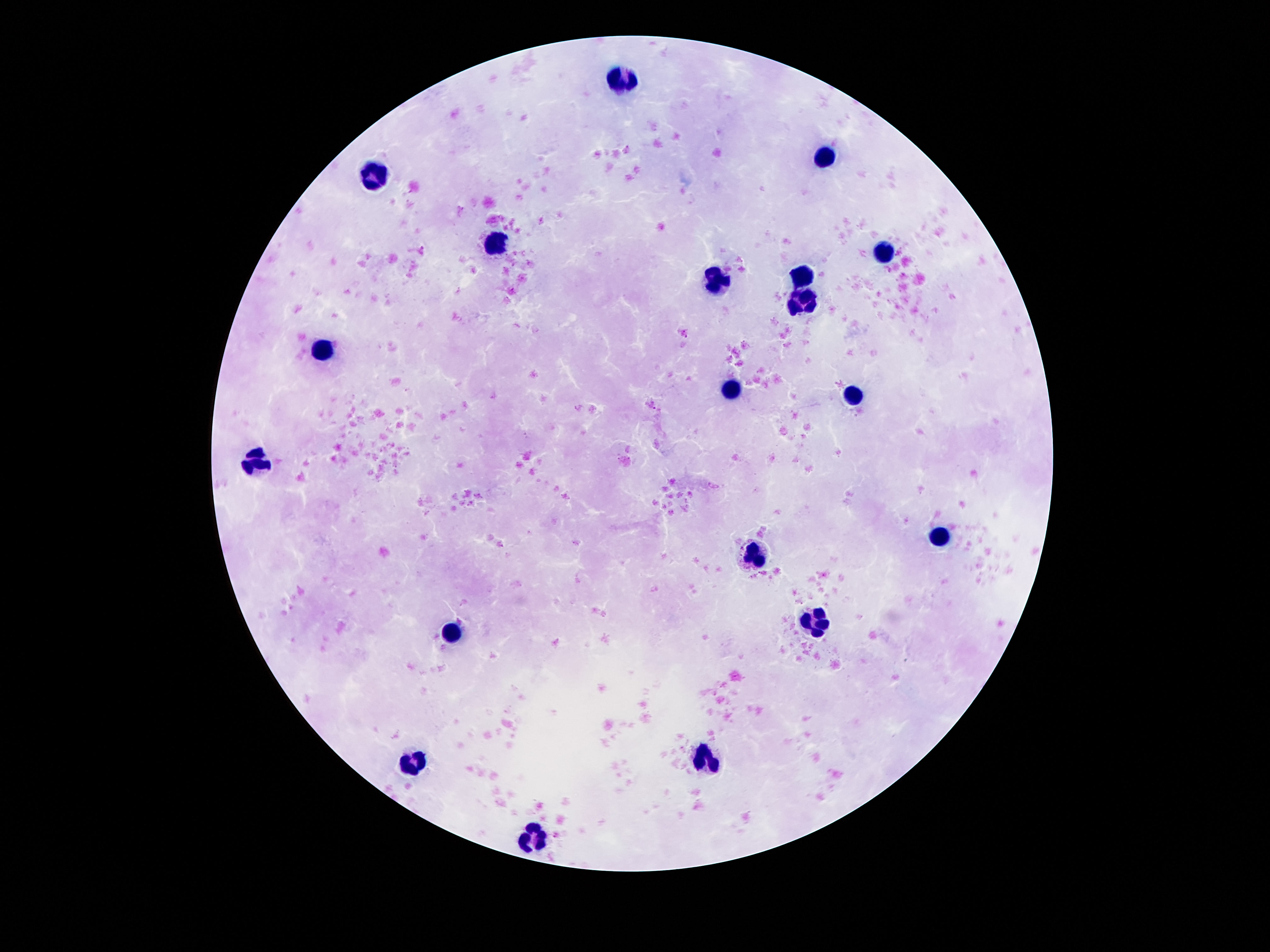

Approximate centers as {x, y} in pixels. Leukocyte locations: {622, 77}, {826, 160}, {375, 173}, {495, 242}, {885, 253}, {801, 274}, {715, 282}, {803, 300}, {325, 346}, {731, 387}, {853, 394}, {259, 460}, {944, 538}, {755, 554}, {815, 620}, {454, 632}, {706, 759}, {413, 766}, {529, 840}. Patient malaria status: uninfected. 100x magnification. Thick peripheral-blood smear. Single field of view. Image is 1270×952 pixels. Photographed through the microscope eyepiece with a smartphone camera. Giemsa-stained preparation.